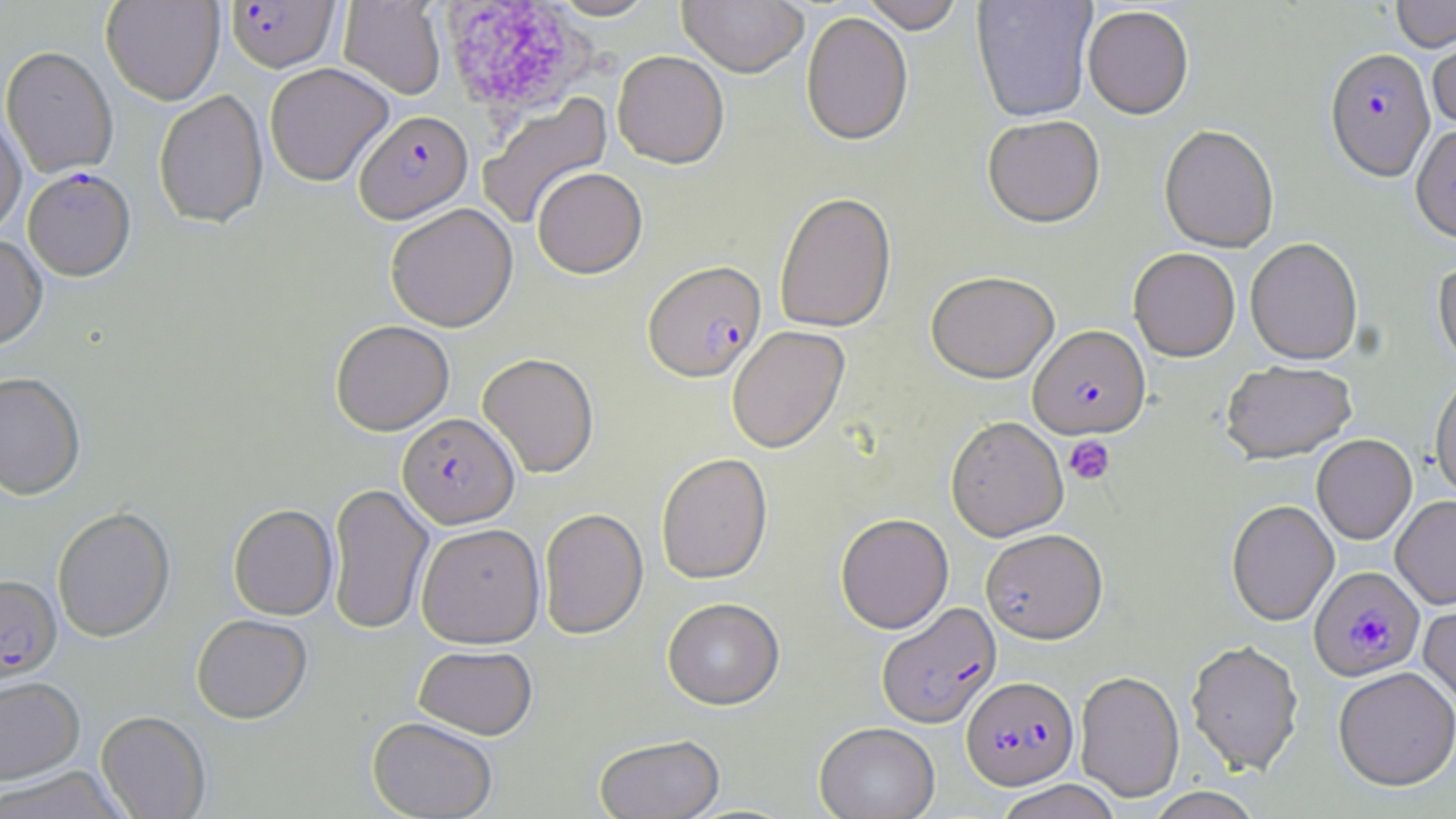
Approximate bounding boxes as named x1/y1/x2/y2 corners in pixels. Uninfected red blood cell locations (subset): (x1=101, y1=0, x2=224, y2=105), (x1=338, y1=0, x2=446, y2=100), (x1=548, y1=0, x2=661, y2=21), (x1=677, y1=0, x2=809, y2=78), (x1=860, y1=0, x2=965, y2=35), (x1=971, y1=0, x2=1097, y2=124), (x1=1391, y1=0, x2=1455, y2=53), (x1=1082, y1=7, x2=1194, y2=122), (x1=801, y1=12, x2=913, y2=148), (x1=1428, y1=33, x2=1456, y2=133), (x1=1, y1=45, x2=118, y2=178), (x1=612, y1=51, x2=729, y2=169), (x1=264, y1=62, x2=394, y2=187), (x1=153, y1=89, x2=269, y2=229), (x1=477, y1=92, x2=614, y2=232), (x1=0, y1=110, x2=27, y2=239), (x1=982, y1=118, x2=1105, y2=230), (x1=1158, y1=127, x2=1279, y2=255), (x1=532, y1=167, x2=648, y2=279), (x1=774, y1=192, x2=897, y2=334), (x1=385, y1=203, x2=518, y2=331), (x1=0, y1=234, x2=48, y2=351), (x1=1245, y1=240, x2=1363, y2=368), (x1=1128, y1=249, x2=1240, y2=364), (x1=1432, y1=259, x2=1456, y2=376), (x1=926, y1=274, x2=1060, y2=385), (x1=330, y1=320, x2=454, y2=435), (x1=727, y1=326, x2=850, y2=454), (x1=477, y1=352, x2=599, y2=478), (x1=1220, y1=364, x2=1358, y2=467), (x1=0, y1=371, x2=86, y2=500), (x1=1430, y1=374, x2=1456, y2=502), (x1=945, y1=417, x2=1069, y2=542), (x1=1312, y1=436, x2=1417, y2=545), (x1=656, y1=453, x2=772, y2=584), (x1=327, y1=482, x2=434, y2=635), (x1=1391, y1=497, x2=1456, y2=610), (x1=1226, y1=501, x2=1339, y2=628), (x1=228, y1=503, x2=338, y2=620), (x1=52, y1=506, x2=176, y2=642), (x1=539, y1=508, x2=648, y2=639), (x1=835, y1=513, x2=954, y2=634), (x1=416, y1=522, x2=545, y2=648), (x1=980, y1=530, x2=1108, y2=646), (x1=1418, y1=596, x2=1456, y2=714), (x1=662, y1=598, x2=785, y2=710), (x1=191, y1=614, x2=312, y2=724), (x1=1186, y1=641, x2=1304, y2=777), (x1=413, y1=645, x2=537, y2=739), (x1=1333, y1=669, x2=1456, y2=793), (x1=1075, y1=671, x2=1185, y2=803), (x1=0, y1=676, x2=85, y2=784), (x1=95, y1=710, x2=211, y2=819), (x1=367, y1=716, x2=498, y2=818), (x1=814, y1=723, x2=939, y2=819), (x1=593, y1=734, x2=725, y2=818), (x1=0, y1=766, x2=131, y2=819), (x1=993, y1=780, x2=1123, y2=819), (x1=1144, y1=788, x2=1264, y2=818). Plasmodium falciparum-infected red blood cell locations (subset): (x1=225, y1=1, x2=340, y2=73), (x1=1324, y1=52, x2=1436, y2=185), (x1=354, y1=110, x2=473, y2=224), (x1=23, y1=167, x2=135, y2=281), (x1=642, y1=260, x2=766, y2=383), (x1=1027, y1=327, x2=1150, y2=441), (x1=397, y1=412, x2=519, y2=528), (x1=1309, y1=566, x2=1426, y2=683), (x1=0, y1=574, x2=62, y2=684), (x1=876, y1=603, x2=1001, y2=730), (x1=962, y1=676, x2=1079, y2=791). Platelet locations: (x1=436, y1=1, x2=595, y2=119), (x1=1064, y1=436, x2=1115, y2=486). Slide-level diagnosis: Plasmodium falciparum. Thin blood smear. Image is 1456×819 pixels. Captured at 1000x magnification. May-Grünwald-Giemsa-stained preparation. Light microscopy. One field of a larger specimen.